Classify this cell by malaria status.
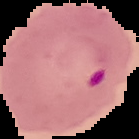

It is parasitized.

Summary:
  - Image size: 139×139 pixels
  - Image type: segmented cell region on a black background
  - Preparation: thin blood smear